Outline each blood parasite and name the species.
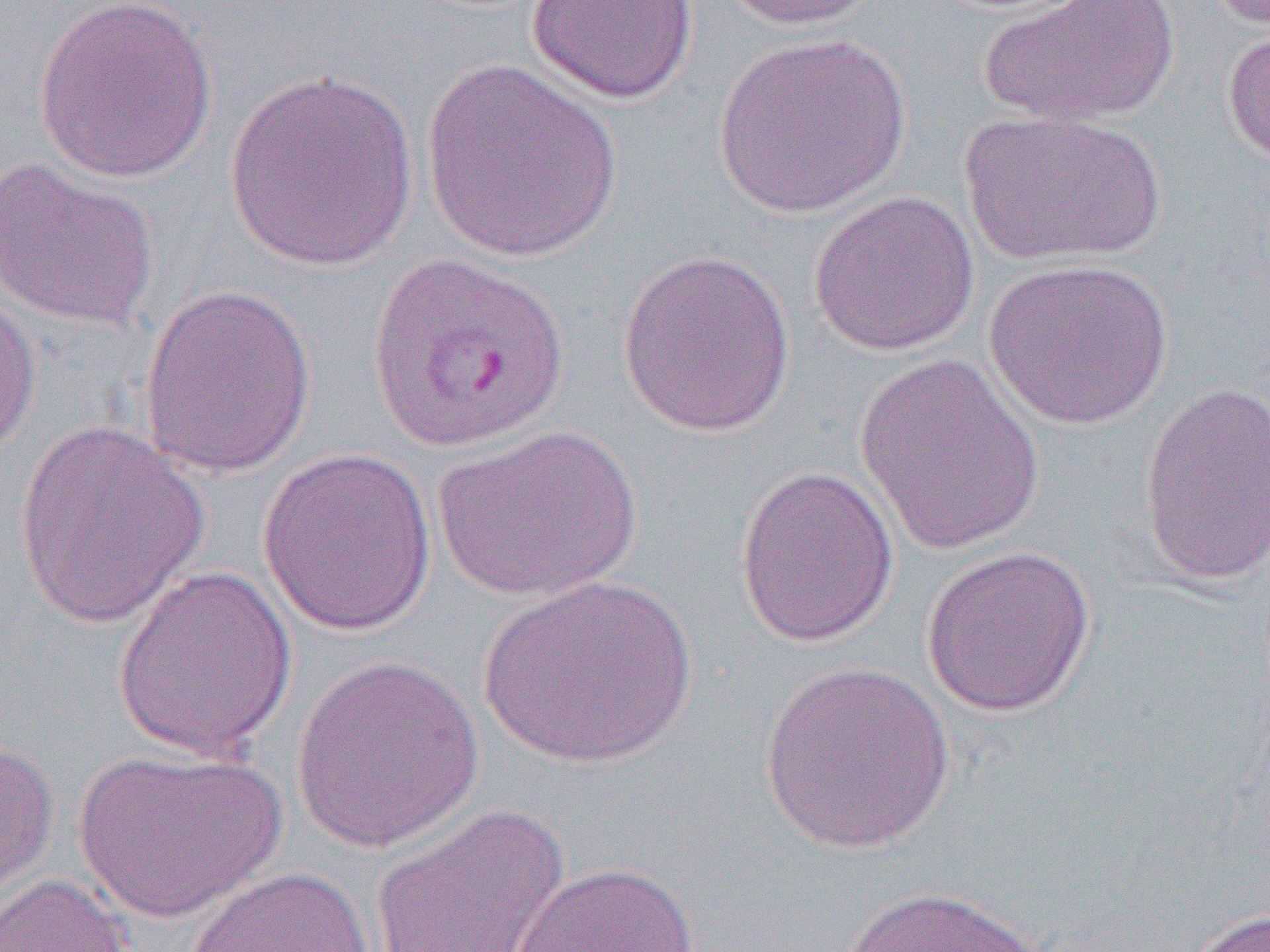
Approximate bounding boxes as (x1,y1)-(x2,y2) corner pairs in pixels.
Plasmodium vivax-infected red blood cells: (367,250)-(570,455).
No Plasmodium falciparum, Plasmodium ovale, Plasmodium malariae, Babesia divergens, or Trypanosoma brucei observed.

{
  "slide_level_diagnosis": "Plasmodium vivax",
  "preparation": "thin blood film",
  "modality": "light microscopy",
  "image_size": "1270×952 pixels",
  "field_of_view": "one of a larger specimen",
  "uninfected_red_blood_cell_locations": "approximate bounding boxes as (x1,y1)-(x2,y2) corner pairs in pixels: (32,0)-(218,184), (721,0)-(884,32), (976,0)-(1180,128), (526,1)-(699,105), (1221,23)-(1270,169), (712,33)-(913,218), (420,58)-(624,264), (223,68)-(420,272), (959,110)-(1165,266), (0,157)-(160,332), (808,189)-(980,357), (617,248)-(796,438), (983,257)-(1175,430), (137,282)-(316,478), (0,292)-(41,463), (853,353)-(1045,554), (1135,381)-(1270,588), (15,419)-(209,629), (432,423)-(641,603), (257,447)-(438,638), (734,464)-(900,648), (921,544)-(1097,718), (112,563)-(299,761), (476,575)-(699,770), (290,654)-(485,853), (758,660)-(956,854), (0,737)-(59,908), (73,747)-(285,924), (369,803)-(570,952), (507,861)-(701,952), (182,865)-(376,952), (0,872)-(132,952), (837,884)-(1052,952), (1186,907)-(1270,952)",
  "magnification": "1000x"
}